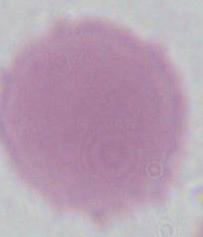

Summary:
  - Identification: red blood cell
  - Modality: photomicrograph
  - Magnification: 1000x